Assess this cell for malaria.
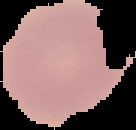
It is uninfected.

Cell region segmented out of the field of view; the surrounding area is masked to black. Image is 136×130 pixels. From a thin blood smear.